Outline each uninfected red blood cell.
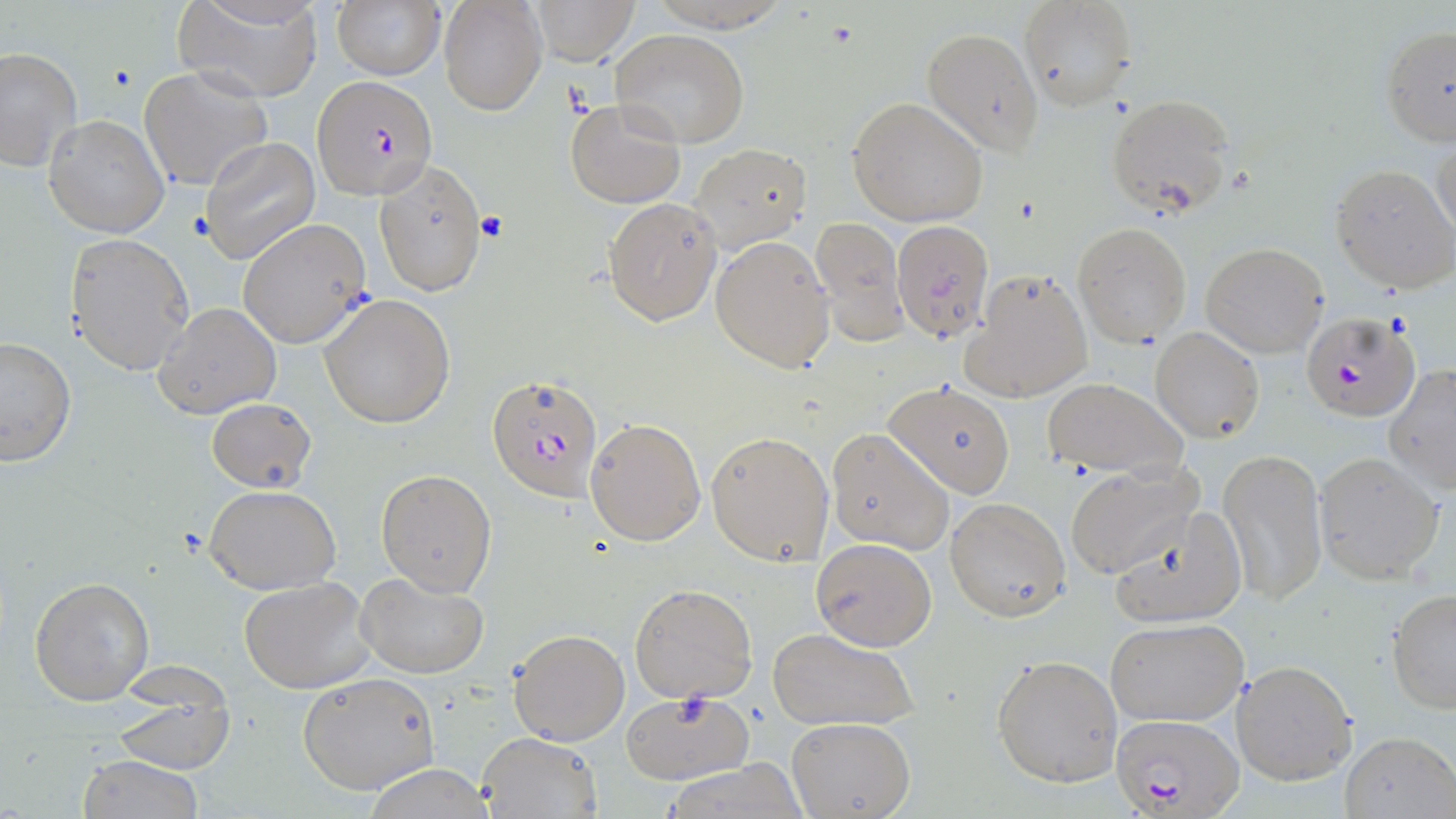

Approximate bounding boxes as (x1,y1)-(x2,y2) corner pairs in pixels.
Uninfected red blood cells: (529,0)-(640,65), (1018,0)-(1135,111), (438,1)-(547,115), (643,1)-(792,32), (175,2)-(324,102), (330,2)-(445,82), (1379,25)-(1456,148), (920,27)-(1044,156), (611,29)-(749,147), (0,47)-(80,172), (139,66)-(274,192), (1107,92)-(1237,219), (847,96)-(990,227), (564,99)-(688,208), (44,114)-(169,238), (1432,136)-(1456,241), (199,137)-(321,266), (692,143)-(812,253), (374,161)-(487,298), (1330,162)-(1456,292), (603,197)-(723,323), (238,219)-(372,348), (806,219)-(908,341), (891,220)-(995,345), (1073,222)-(1192,346), (65,232)-(195,376), (711,236)-(836,373), (1202,242)-(1329,356), (963,270)-(1093,402), (319,293)-(457,429), (153,301)-(282,420), (1150,326)-(1264,444), (0,335)-(78,465), (1384,364)-(1456,495), (884,379)-(1017,498), (1040,379)-(1185,479), (206,398)-(316,492), (586,417)-(706,546), (825,427)-(955,555), (706,429)-(834,566), (1217,447)-(1328,606), (1315,453)-(1445,583), (1065,462)-(1202,579), (375,468)-(497,596), (205,485)-(341,595), (945,497)-(1070,621), (1108,507)-(1247,630), (811,538)-(937,652), (358,571)-(490,678), (29,574)-(155,706), (238,576)-(376,694), (628,583)-(759,703), (1387,588)-(1456,713), (1106,618)-(1248,727), (767,626)-(918,732), (509,628)-(629,746), (991,653)-(1123,788), (1232,659)-(1357,785), (298,672)-(439,794), (620,692)-(753,784), (112,697)-(234,773), (787,718)-(914,818), (476,730)-(602,818), (1339,730)-(1456,819), (77,755)-(206,818), (658,761)-(815,817), (359,767)-(496,819).

Summary:
  - Plasmodium falciparum-infected red blood cell locations: (312,75)-(439,200), (1302,311)-(1420,422), (486,372)-(608,504), (1113,711)-(1245,817)
  - Platelet locations: (476,210)-(509,245)
  - Slide-level diagnosis: Plasmodium falciparum
  - Preparation: thin blood film
  - Image size: 1456×819 pixels
  - Modality: optical microscopy
  - Magnification: 1000x
  - Field of view: single
  - Stain: May-Grünwald-Giemsa